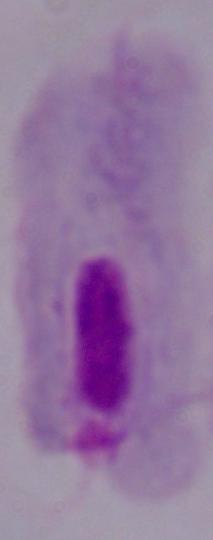

Summary:
  - Magnification: 1000x
  - Modality: micrograph
  - Identification: trichomonad